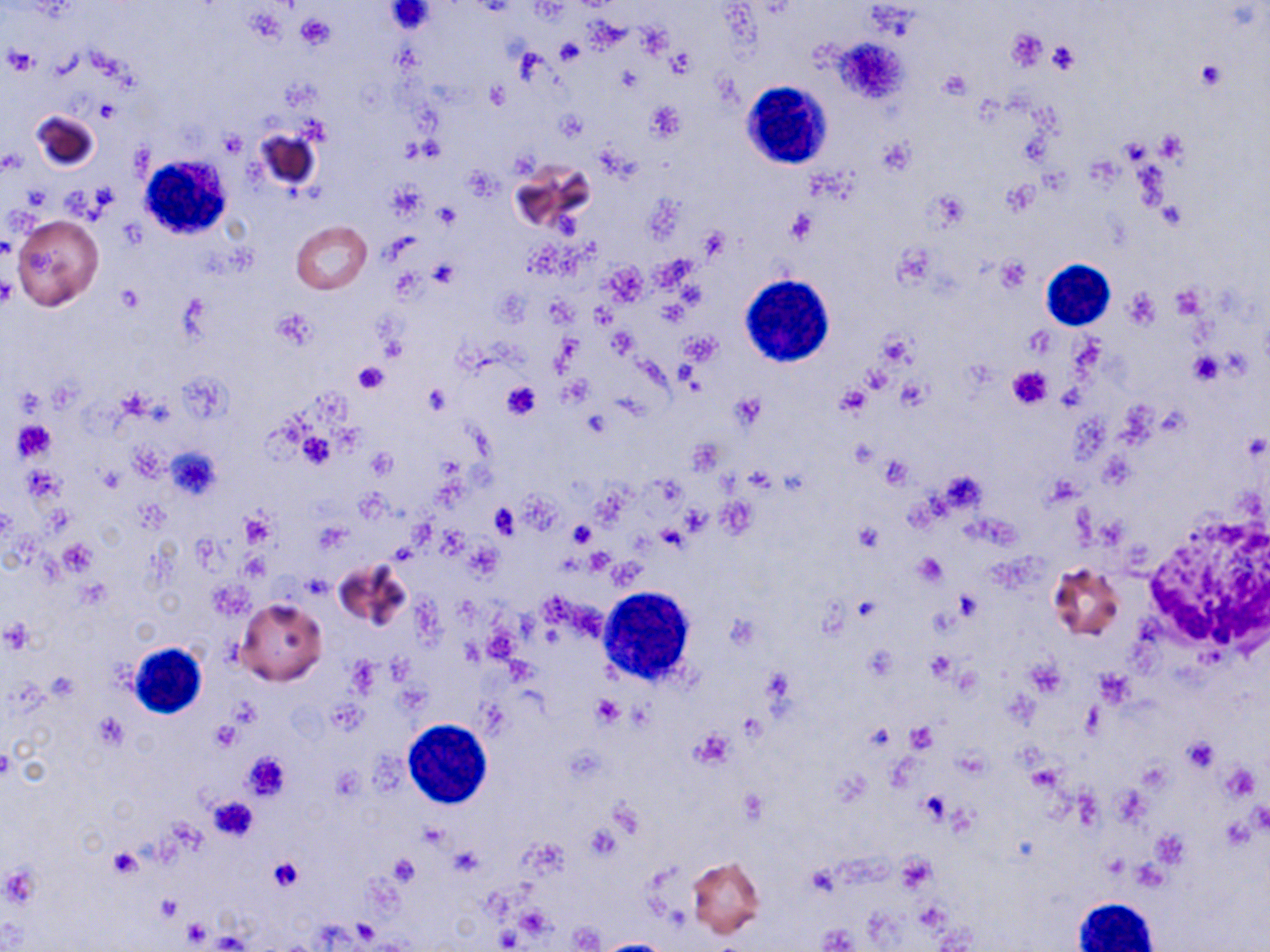

Summary:
  - Coordinate format: approximate bounding boxes as [x1, y1, x2, y2] in pixels
  - White blood cell locations: [740, 81, 830, 169], [140, 155, 232, 238], [1042, 260, 1115, 330], [740, 275, 835, 367], [599, 585, 697, 688], [126, 640, 208, 720], [403, 719, 492, 808], [1074, 901, 1156, 951]
  - Platelet locations: [385, 1, 437, 35], [295, 13, 334, 50], [637, 25, 672, 55], [1005, 31, 1047, 72], [833, 37, 911, 107], [555, 38, 585, 64], [1046, 42, 1080, 74], [4, 45, 35, 75], [669, 48, 693, 77], [1195, 59, 1224, 90], [939, 70, 970, 98], [485, 83, 508, 110], [96, 101, 121, 123], [646, 102, 685, 141], [558, 111, 588, 141], [1153, 131, 1187, 164], [220, 133, 245, 156], [879, 137, 913, 173], [463, 168, 498, 199], [1002, 178, 1038, 215], [387, 182, 427, 219], [433, 204, 460, 229], [1159, 205, 1186, 229], [785, 208, 817, 245], [699, 227, 731, 261], [995, 257, 1030, 289], [430, 259, 459, 286], [1169, 285, 1207, 320], [114, 287, 143, 314], [1123, 289, 1161, 328], [271, 307, 318, 350], [609, 328, 637, 354], [681, 333, 719, 364], [876, 334, 913, 370], [1189, 352, 1222, 383], [352, 360, 389, 395], [1007, 366, 1053, 409], [560, 379, 592, 407], [499, 380, 542, 420], [424, 384, 452, 414], [835, 385, 872, 416], [730, 393, 765, 428], [14, 421, 55, 460], [297, 433, 335, 469], [165, 447, 221, 499], [367, 448, 398, 477], [491, 504, 519, 537], [680, 506, 709, 534], [242, 512, 275, 546], [854, 521, 883, 552], [569, 522, 596, 547], [657, 524, 687, 551], [59, 540, 97, 575], [586, 549, 613, 576], [915, 552, 947, 586], [722, 612, 760, 651], [2, 619, 33, 652], [925, 651, 954, 683], [1025, 661, 1066, 698], [1094, 670, 1133, 703], [591, 695, 623, 727], [209, 721, 242, 752], [905, 724, 937, 752], [690, 729, 735, 768], [1181, 737, 1218, 772], [241, 750, 291, 801], [919, 791, 951, 823], [207, 797, 259, 841], [1250, 804, 1270, 831], [107, 847, 143, 877], [390, 853, 419, 885], [269, 858, 304, 891], [3, 865, 41, 907], [156, 895, 183, 923], [182, 919, 210, 947]
  - Uninfected red blood cell locations: [33, 111, 99, 171], [255, 128, 322, 193], [512, 159, 593, 234], [11, 213, 104, 310], [290, 221, 371, 295], [334, 559, 410, 631], [1048, 563, 1125, 642], [235, 598, 328, 685], [687, 857, 765, 939]
  - Slide-level diagnosis: no evidence of blood parasites
  - Field of view: one of a larger specimen
  - Image size: 1270×952 pixels
  - Modality: light microscopy
  - Stain: May-Grünwald-Giemsa
  - Preparation: thin blood smear
  - Magnification: 1000x